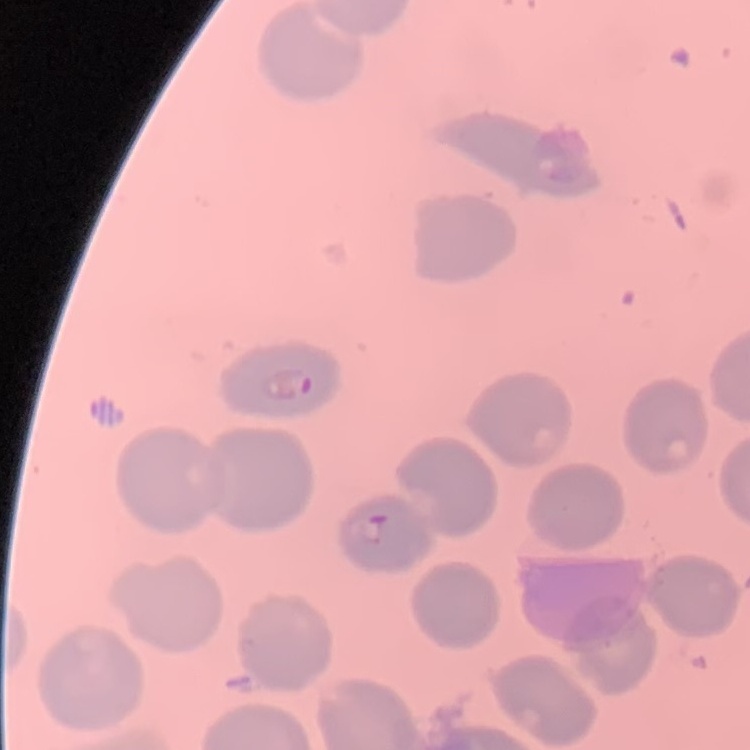

Summary:
  - Red blood cell morphology: no rouleaux formation
  - Preparation: thin blood smear
  - Stain: Field's or Giemsa
  - Image type: one tile cut from a larger photomicrograph